Classify this cell by malaria status.
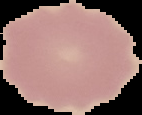

Uninfected.

{
  "image_size": "142×115 pixels",
  "image_type": "cell region segmented out of the field of view; surrounding area masked to black",
  "preparation": "thin blood film"
}